Report the malaria status of this cell.
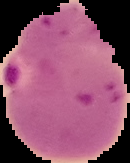
Parasitized.

The area outside the segmented cell region is set to black. From a thin blood film. Image is 130×163 pixels.